Assess this cell for malaria.
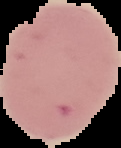

Uninfected.

Summary:
  - Preparation: thin blood film
  - Image size: 121×148 pixels
  - Image type: cell region segmented out of the field of view; surrounding area masked to black